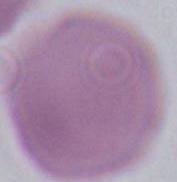 Captured at 1000x magnification. Micrograph. An erythrocyte is shown.